Assess this cell for malaria.
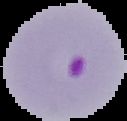

Parasitized.

From a thin blood smear. Image is 127×121 pixels. Segmented cell region on a black background.